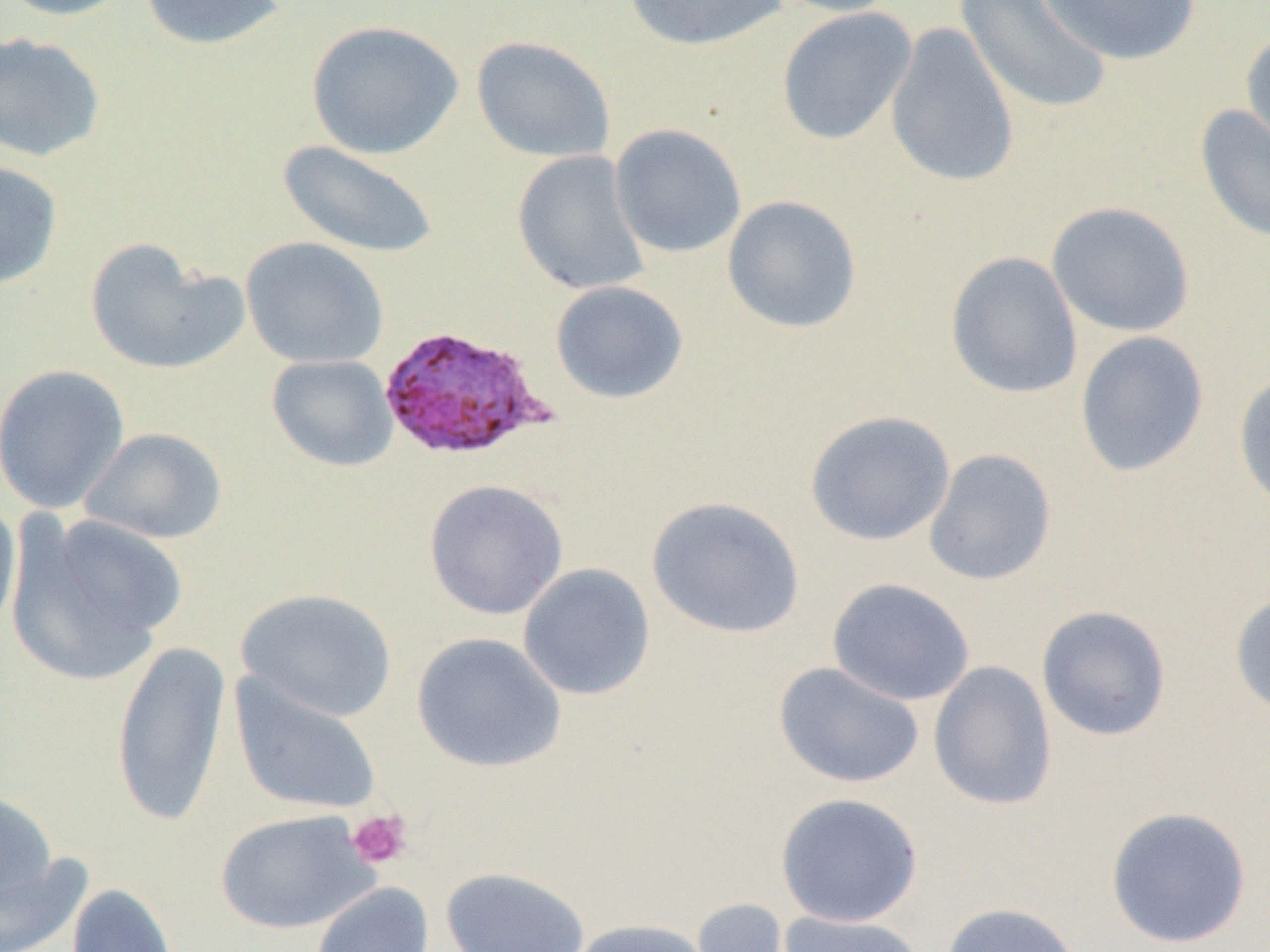

slide-level diagnosis = Plasmodium ovale
modality = light microscopy
platelet locations = approximate bounding boxes as (x1, y1, x2, y2) in pixels: (346, 808, 412, 870)
image size = 1270×952 pixels
magnification = 1000x
field of view = single
preparation = thin blood smear
Plasmodium ovale-infected red blood cell locations = approximate bounding boxes as (x1, y1, x2, y2) in pixels: (377, 324, 553, 462)
uninfected red blood cell locations = approximate bounding boxes as (x1, y1, x2, y2) in pixels: (0, 0, 138, 21), (139, 0, 289, 51), (622, 0, 788, 52), (766, 0, 907, 18), (954, 0, 1113, 115), (1039, 0, 1202, 66), (776, 6, 917, 146), (306, 20, 464, 159), (884, 20, 1021, 189), (1240, 28, 1270, 162), (0, 31, 107, 163), (471, 36, 615, 163), (1194, 105, 1270, 245), (608, 123, 747, 258), (277, 140, 438, 259), (512, 150, 650, 295), (0, 160, 63, 290), (722, 195, 862, 333), (1046, 202, 1196, 338), (240, 236, 389, 369), (84, 238, 246, 377), (945, 250, 1083, 400), (550, 280, 689, 404), (1075, 331, 1209, 477), (266, 354, 398, 472), (0, 364, 131, 513), (1233, 368, 1270, 516), (804, 410, 955, 546), (80, 427, 227, 544), (923, 449, 1057, 586), (423, 479, 569, 621), (646, 495, 805, 639), (0, 498, 21, 640), (7, 513, 186, 684), (517, 563, 656, 701), (826, 578, 975, 706), (235, 588, 398, 723), (1229, 590, 1270, 719), (1036, 605, 1172, 741), (411, 632, 566, 773), (110, 638, 232, 829), (773, 661, 924, 789), (928, 661, 1058, 811), (229, 674, 382, 817), (0, 788, 58, 909), (775, 792, 923, 927), (1104, 806, 1253, 949), (215, 809, 378, 935), (0, 852, 91, 952), (439, 866, 590, 952), (310, 882, 435, 952), (66, 883, 179, 952), (690, 896, 799, 952), (939, 902, 1082, 952), (778, 911, 928, 952), (563, 918, 716, 952)